Assess the morphology of the erythrocytes.
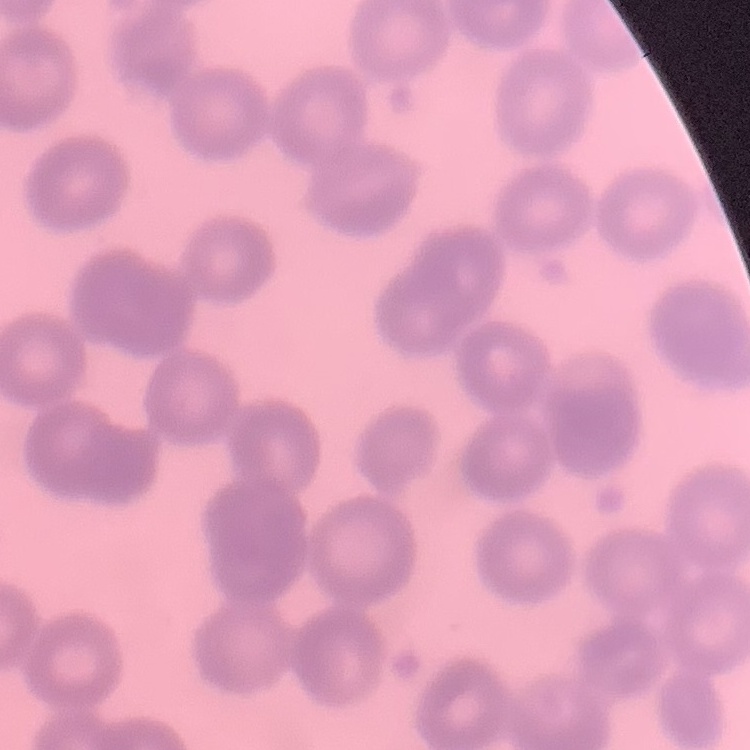

No rouleaux formation.

Summary:
  - Stain: Field's or Giemsa
  - Image type: square crop of a larger photomicrograph
  - Preparation: thin blood film